Report the malaria status of this cell.
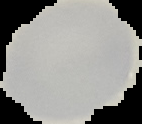

Uninfected.

The area outside the segmented cell region is set to black. From a thin blood film. Image is 142×124 pixels.